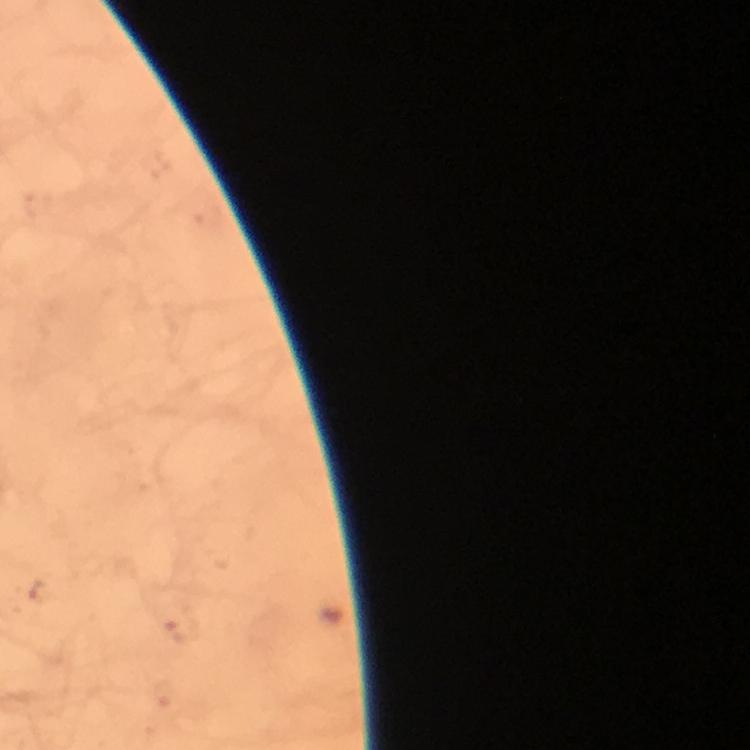

capture = smartphone camera through the microscope
image size = 750×750 pixels
context = from a diagnostic examination for malaria
preparation = thick blood smear
cropped from = a single field of view
immersion oil = applied
malaria parasite locations = approximate centers as [x, y] in pixels: [179, 633], [164, 695]
magnification = 100x
stain = Giemsa